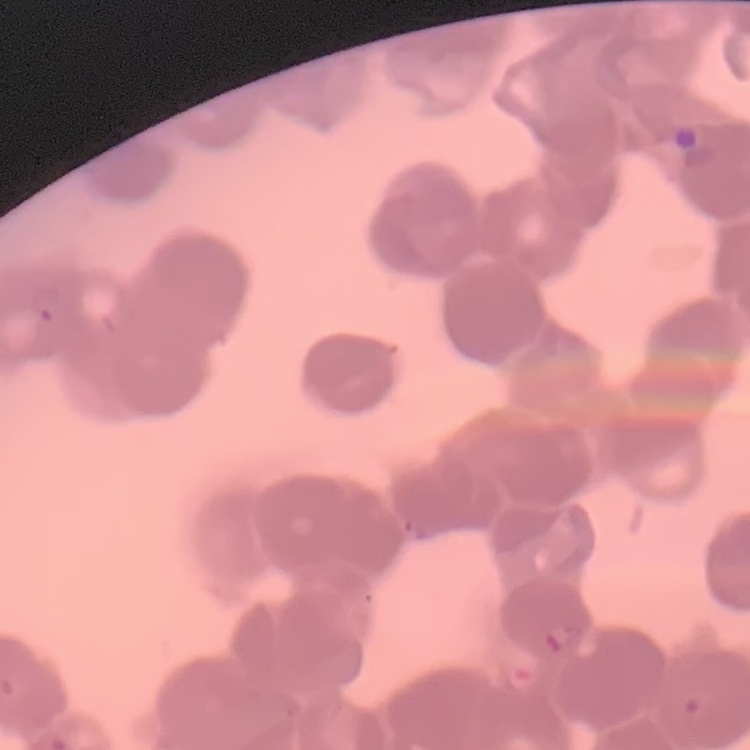
Summary:
  - Erythrocyte morphology: rouleaux formation
  - Image type: square crop of a larger photomicrograph
  - Preparation: thin blood film
  - Stain: Field's or Giemsa